Comment on the morphology of the erythrocytes.
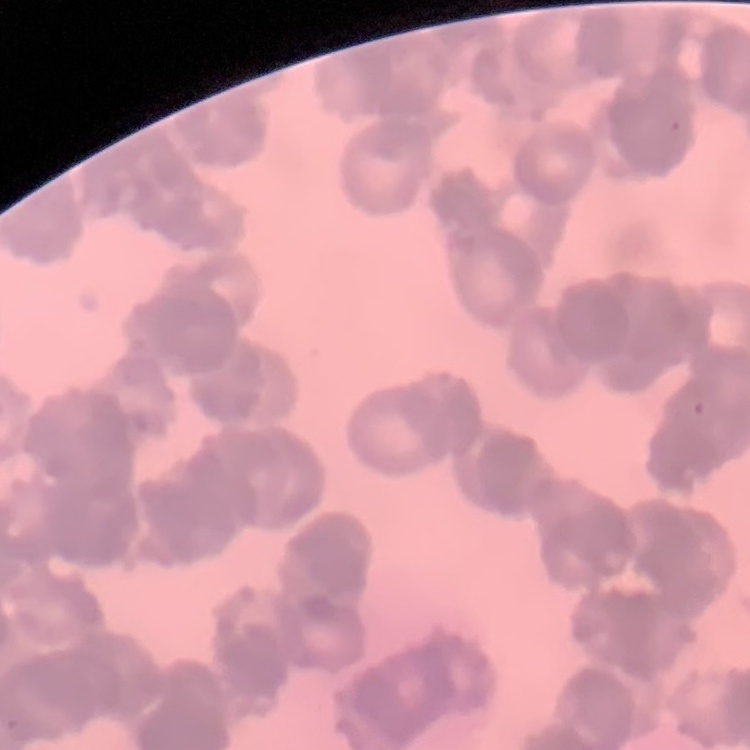

Rouleaux formation.

preparation = thin blood smear
image type = square crop of a larger photomicrograph
stain = Field's or Giemsa